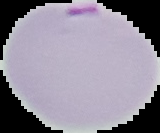

malaria status = parasitized
image type = segmented cell region on a black background
preparation = thin blood smear
image size = 160×133 pixels